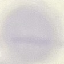
malaria status = uninfected
stain = Giemsa
image type = automatically extracted cell patch, resized to 64 × 64 pixels
preparation = thin blood smear
capture = smartphone camera at the microscope eyepiece